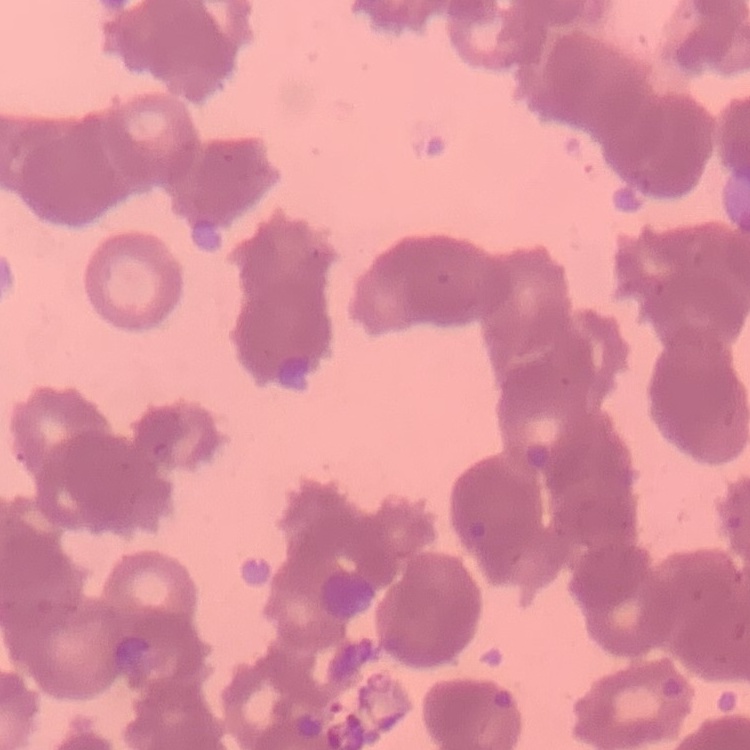 The red blood cells show rouleaux formation. Stained with either Field's or Giemsa. Square crop of a larger photomicrograph. Thin blood film.